Describe the morphology of the erythrocytes.
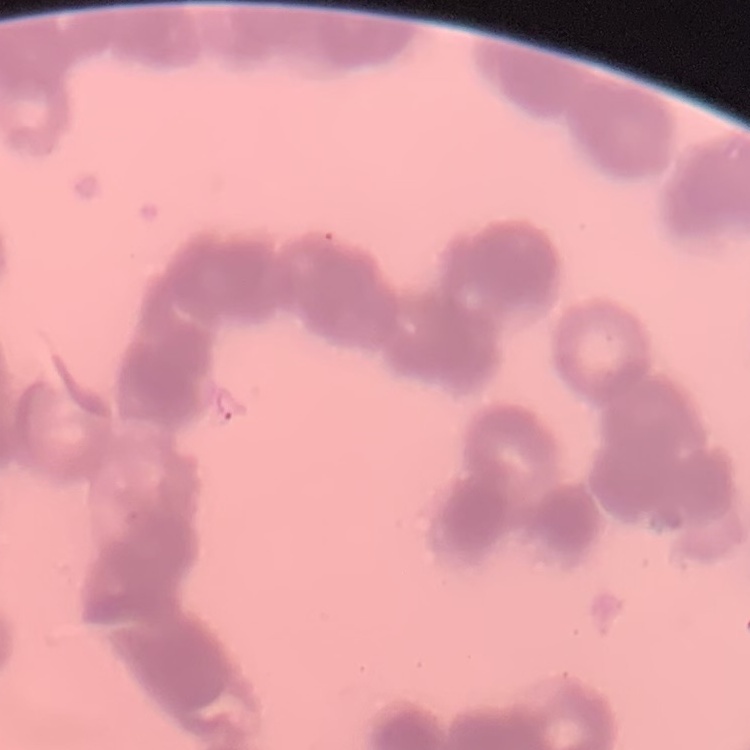
Rouleaux formation.

Square crop of a larger photomicrograph. Field's or Giemsa stain. Thin peripheral smear.